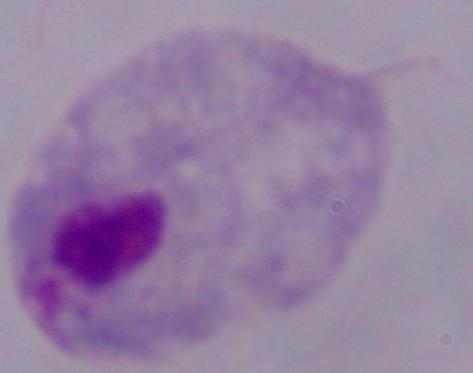
modality = micrograph
magnification = 1000x
identification = trichomonad